Locate every leukocyte (white blood cell).
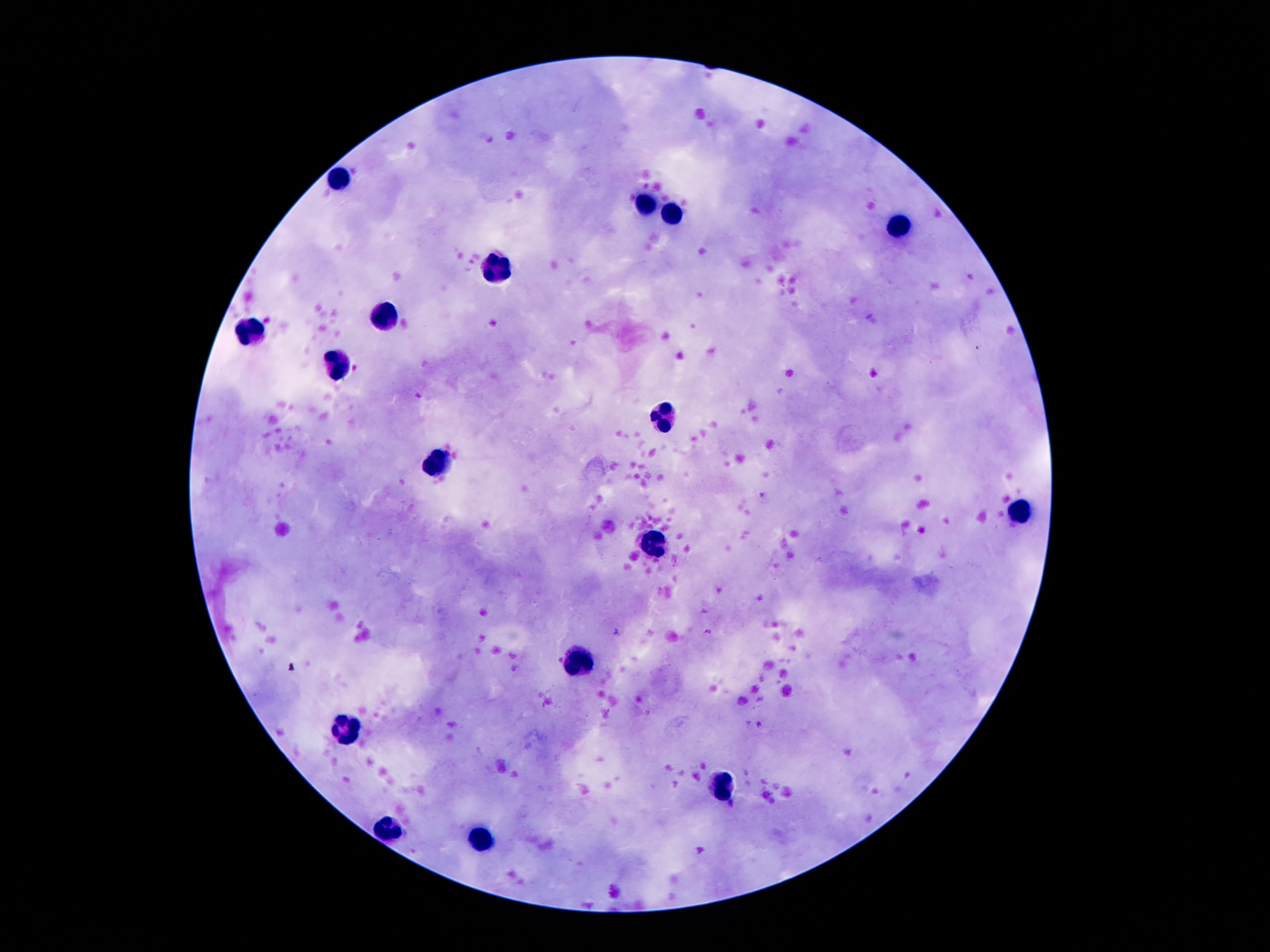
Approximate centers as {x, y} in pixels.
Leukocytes: {338, 182}, {647, 201}, {677, 212}, {895, 221}, {497, 267}, {384, 319}, {248, 333}, {341, 362}, {665, 417}, {441, 459}, {1020, 512}, {656, 541}, {577, 660}, {352, 728}, {722, 787}, {388, 830}, {486, 839}.

{
  "field_of_view": "one from this slide",
  "image_size": "1270×952 pixels",
  "preparation": "thick peripheral-blood smear",
  "patient_malaria_status": "not infected",
  "magnification": "100x",
  "capture": "smartphone camera through the microscope eyepiece",
  "stain": "Giemsa"
}